Give the position of every leukocyte visible.
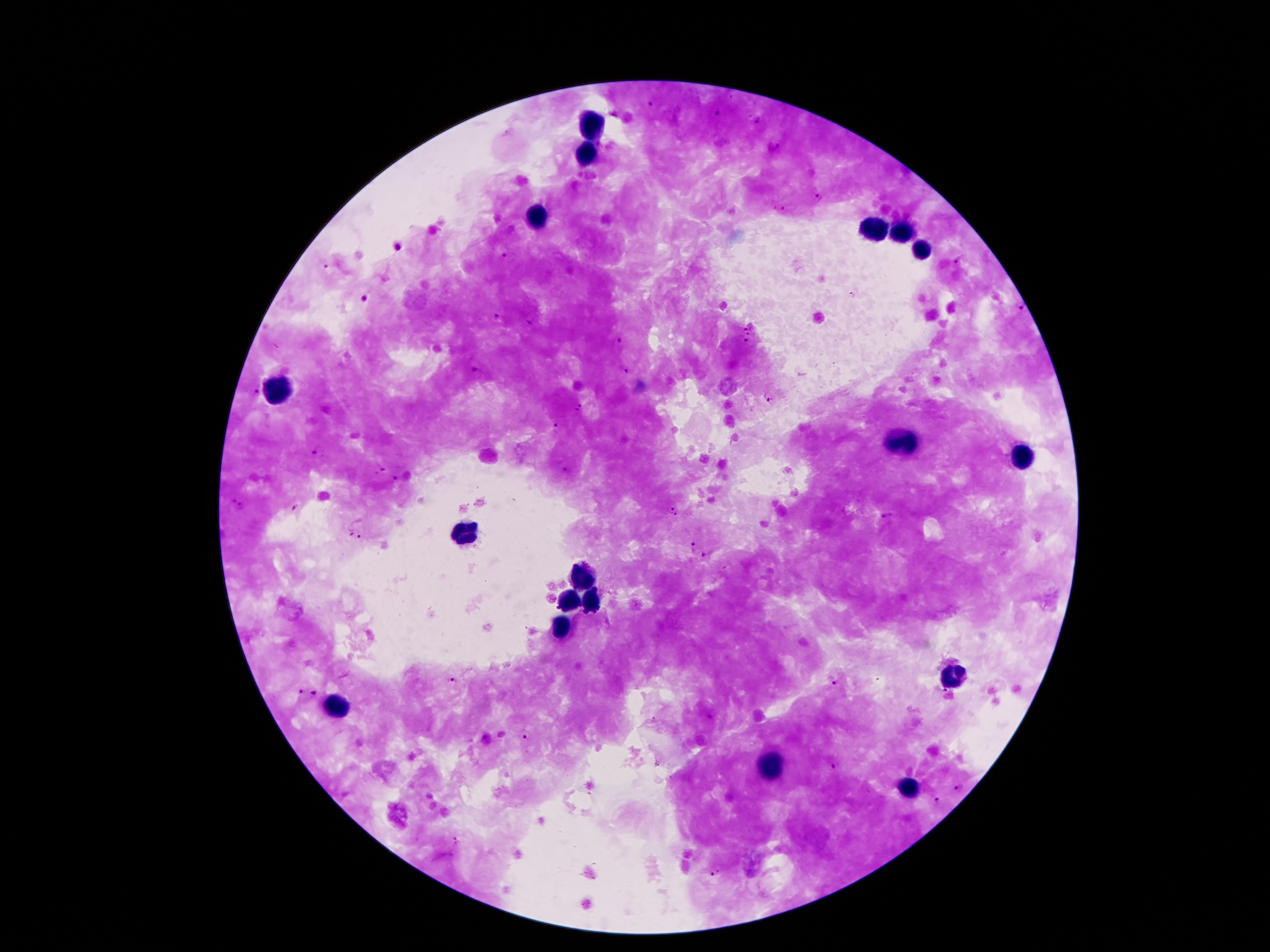
Approximate centers as (x, y) in pixels.
Leukocytes: (589, 123), (584, 159), (536, 213), (870, 230), (906, 230), (923, 249), (278, 388), (904, 442), (1021, 455), (465, 535), (581, 575), (569, 602), (592, 602), (561, 626), (952, 677), (337, 710), (770, 765), (909, 786).

Summary:
  - Plasmodium parasite locations: (651, 104), (715, 113), (759, 121), (507, 133), (777, 147), (819, 197), (779, 208), (398, 248), (508, 256), (956, 262), (327, 268), (854, 295), (365, 300), (1021, 308), (499, 315), (529, 319), (746, 329), (748, 334), (747, 341), (616, 342), (476, 372), (624, 372), (256, 391), (769, 396), (579, 408), (556, 426), (314, 454), (380, 469), (564, 469), (398, 479), (236, 506), (293, 508), (672, 514), (888, 515), (348, 530), (359, 538), (692, 549), (703, 555), (831, 680), (453, 682), (299, 693), (315, 695), (525, 735), (830, 766), (958, 786), (935, 800), (457, 840), (716, 874)
  - Capture: smartphone through the microscope eyepiece
  - Field of view: single
  - Magnification: 100x
  - Preparation: thick blood film
  - Patient malaria status: positive for Plasmodium falciparum
  - Stain: Giemsa
  - Image size: 1270×952 pixels